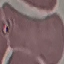 Result: negative for malaria parasites. Photographed with a smartphone camera at the microscope eyepiece. Giemsa stain. Cell patch, automatically extracted from a larger field of view and resized to 64 × 64 pixels. Thin smear of blood.